Point out every malaria parasite.
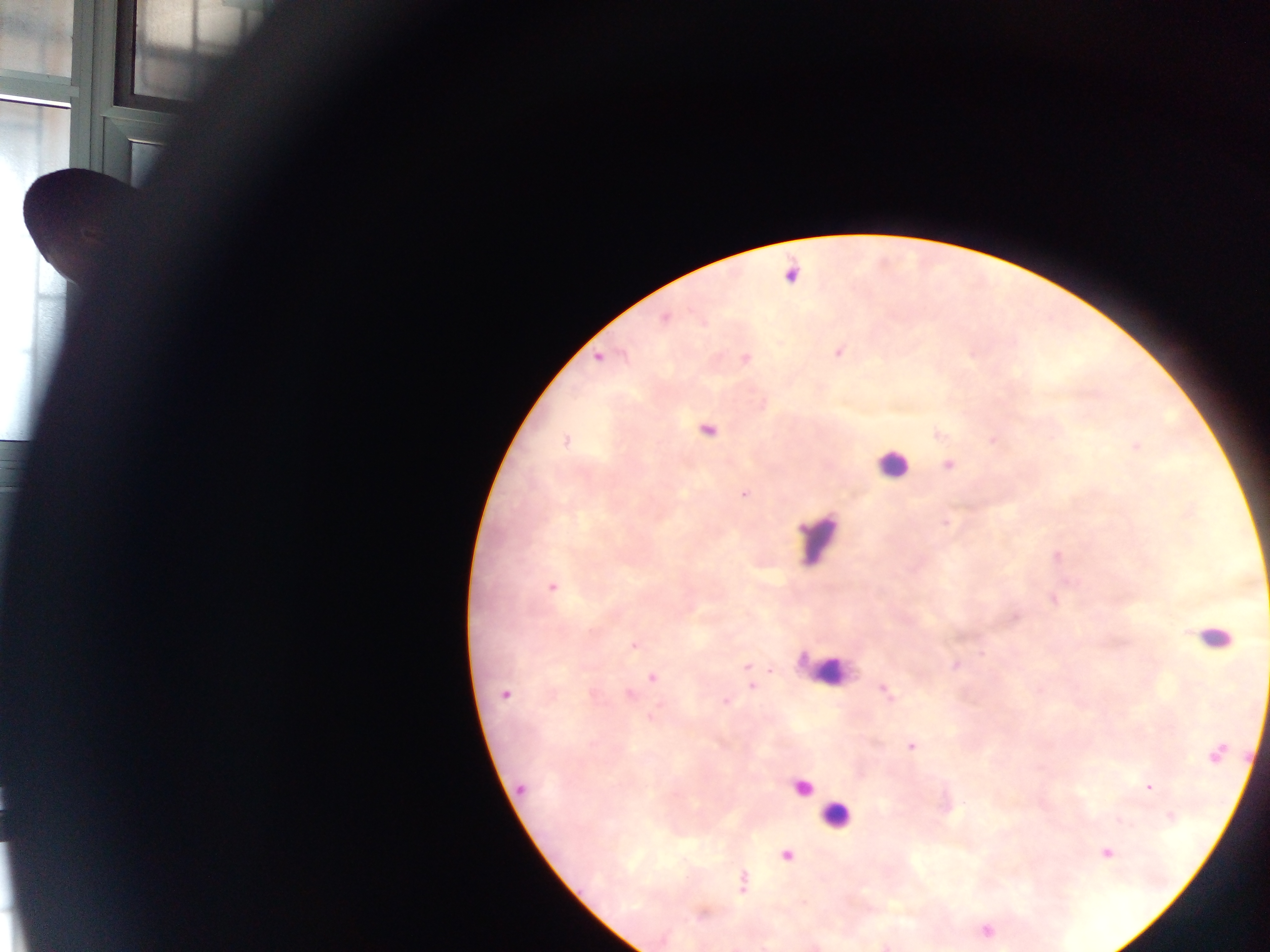
Approximate centers as {x, y} in pixels.
Malaria parasites: {665, 318}, {838, 352}, {599, 358}, {746, 358}, {707, 431}, {566, 442}, {1137, 446}, {949, 465}, {744, 493}, {552, 587}, {634, 645}, {746, 666}, {653, 678}, {751, 687}, {886, 691}, {505, 694}, {629, 694}, {726, 702}, {911, 746}, {1149, 787}, {521, 788}, {1107, 853}, {787, 856}, {742, 882}.

Leukocyte locations: {891, 464}, {818, 538}, {1213, 636}, {822, 671}, {802, 788}, {835, 816}. Sample from Ghana. Image is 1270×952 pixels. Thick blood film. Single field of view. Photographed through a microscope with a mobile-phone camera.